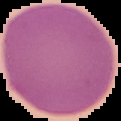
Malaria status: uninfected. Image is 121×121 pixels. The area outside the segmented cell region is set to black. From a thin blood smear.